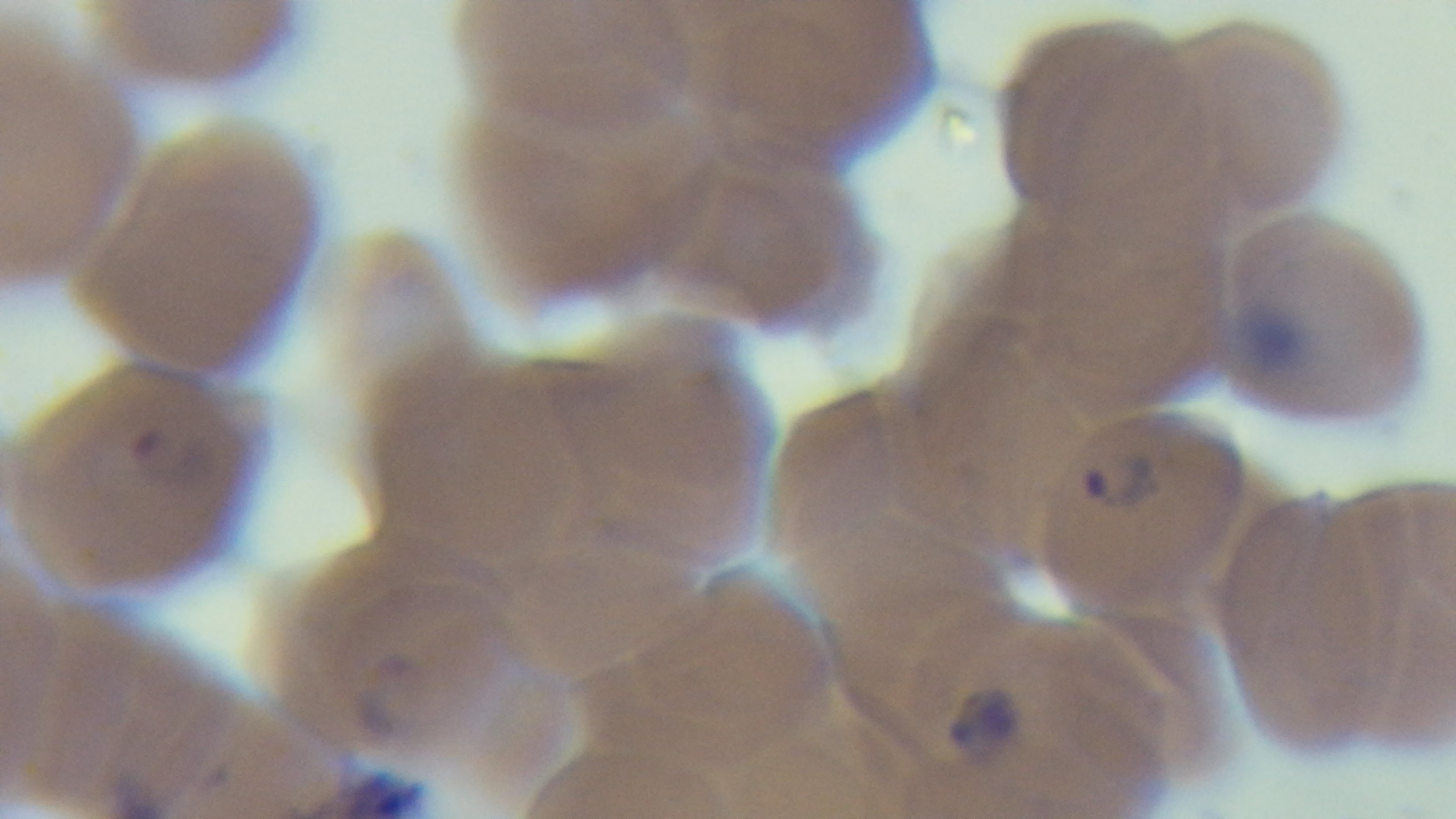
capture = mounted 4K digital camera
malaria status = positive
preparation = thin smear
modality = light microscopy
stain = Giemsa
objective = 100x oil immersion
field of view = single